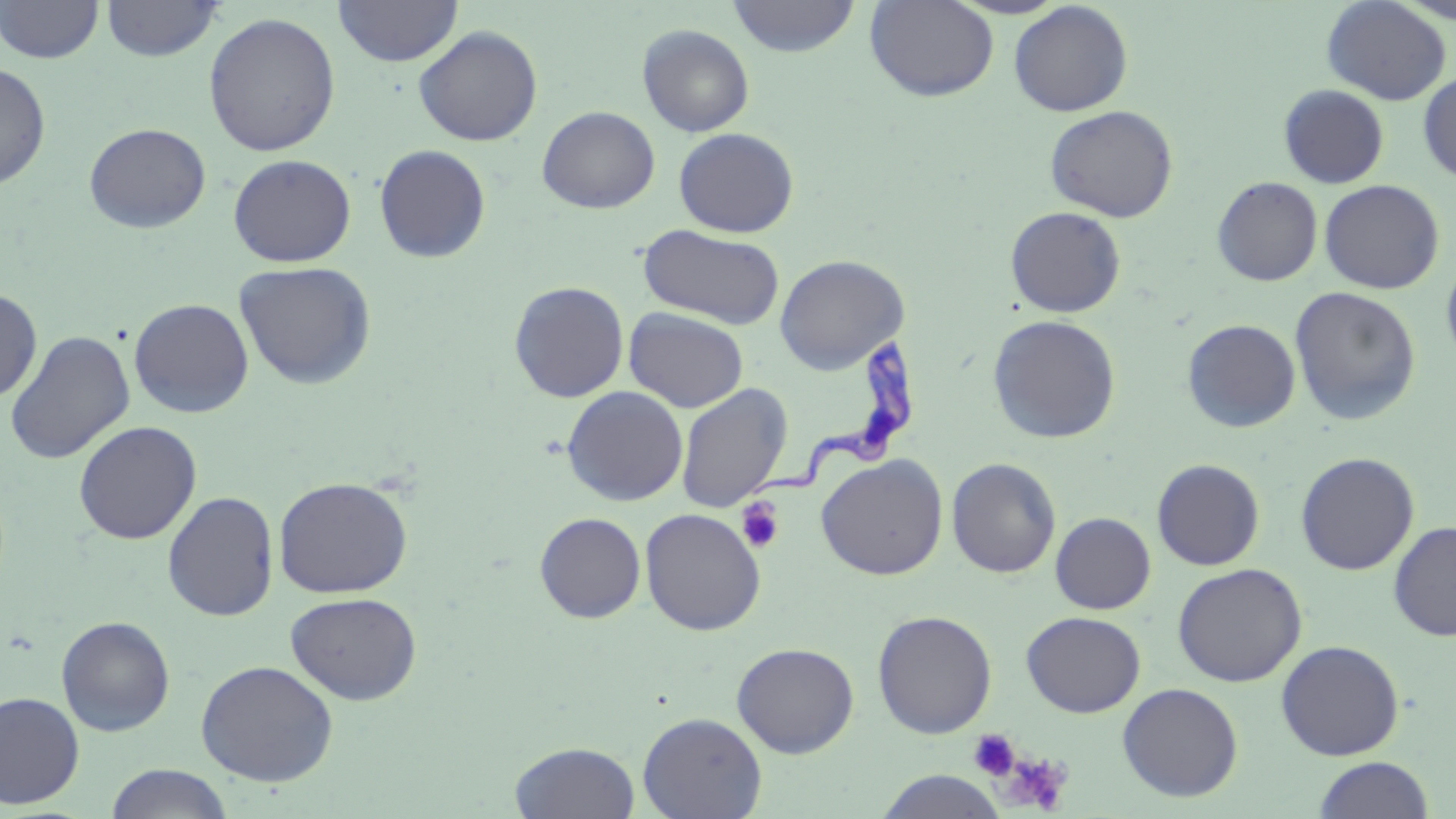
Summary:
  - Coordinate format: approximate bounding boxes as [x1, y1, x2, y2] in pixels
  - Uninfected red blood cell locations: [1, 0, 104, 64], [100, 0, 225, 61], [333, 0, 463, 67], [727, 0, 861, 58], [865, 0, 999, 102], [1321, 0, 1451, 105], [1008, 2, 1133, 116], [203, 12, 341, 157], [637, 24, 754, 137], [413, 26, 543, 145], [0, 60, 51, 190], [1418, 71, 1456, 184], [1279, 85, 1389, 188], [1044, 105, 1178, 222], [537, 106, 660, 213], [83, 122, 211, 233], [673, 127, 799, 238], [374, 144, 491, 263], [228, 154, 357, 267], [1212, 176, 1323, 286], [1319, 179, 1444, 294], [1005, 206, 1126, 318], [638, 224, 785, 330], [774, 254, 909, 374], [1441, 254, 1456, 370], [233, 260, 377, 390], [508, 281, 629, 403], [1289, 286, 1421, 425], [0, 287, 42, 403], [128, 298, 254, 418], [624, 307, 748, 413], [986, 314, 1122, 444], [1182, 319, 1301, 433], [4, 330, 135, 464], [675, 383, 792, 512], [562, 386, 688, 506], [74, 420, 202, 544], [1295, 452, 1419, 575], [816, 454, 949, 580], [947, 458, 1061, 578], [1151, 459, 1265, 570], [273, 476, 413, 599], [162, 491, 279, 621], [640, 508, 767, 636], [534, 512, 646, 623], [1050, 512, 1156, 614], [1388, 520, 1456, 642], [1171, 562, 1307, 687], [285, 592, 422, 705], [872, 609, 997, 738], [1021, 611, 1146, 717], [56, 616, 175, 737], [1276, 639, 1405, 761], [732, 642, 859, 758], [195, 659, 339, 786], [1117, 682, 1243, 802], [0, 691, 85, 809], [637, 711, 767, 819], [509, 741, 640, 818], [1311, 755, 1434, 818], [105, 764, 235, 819], [874, 770, 1008, 819]
  - Platelet locations: [736, 497, 785, 553], [968, 729, 1020, 781], [996, 750, 1073, 814]
  - Trypanosoma brucei locations: [749, 340, 916, 495]
  - Slide-level diagnosis: Trypanosoma brucei
  - Modality: light microscopy
  - Field of view: single
  - Image size: 1456×819 pixels
  - Stain: May-Grünwald-Giemsa
  - Preparation: thin blood smear
  - Magnification: 1000x